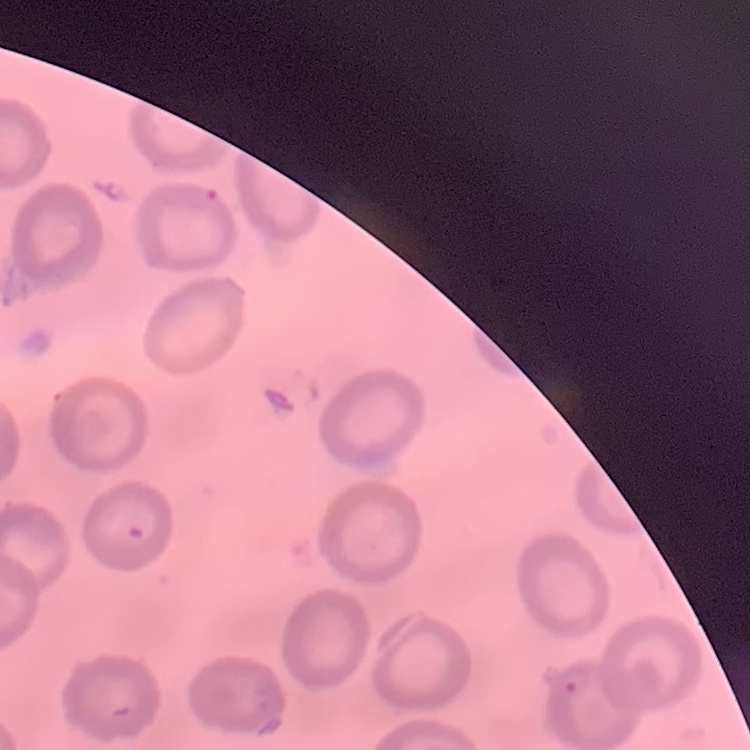
The red blood cells exhibit no rouleaux formation. One tile cut from a larger photomicrograph. Stained with either Field's or Giemsa. Thin peripheral smear.